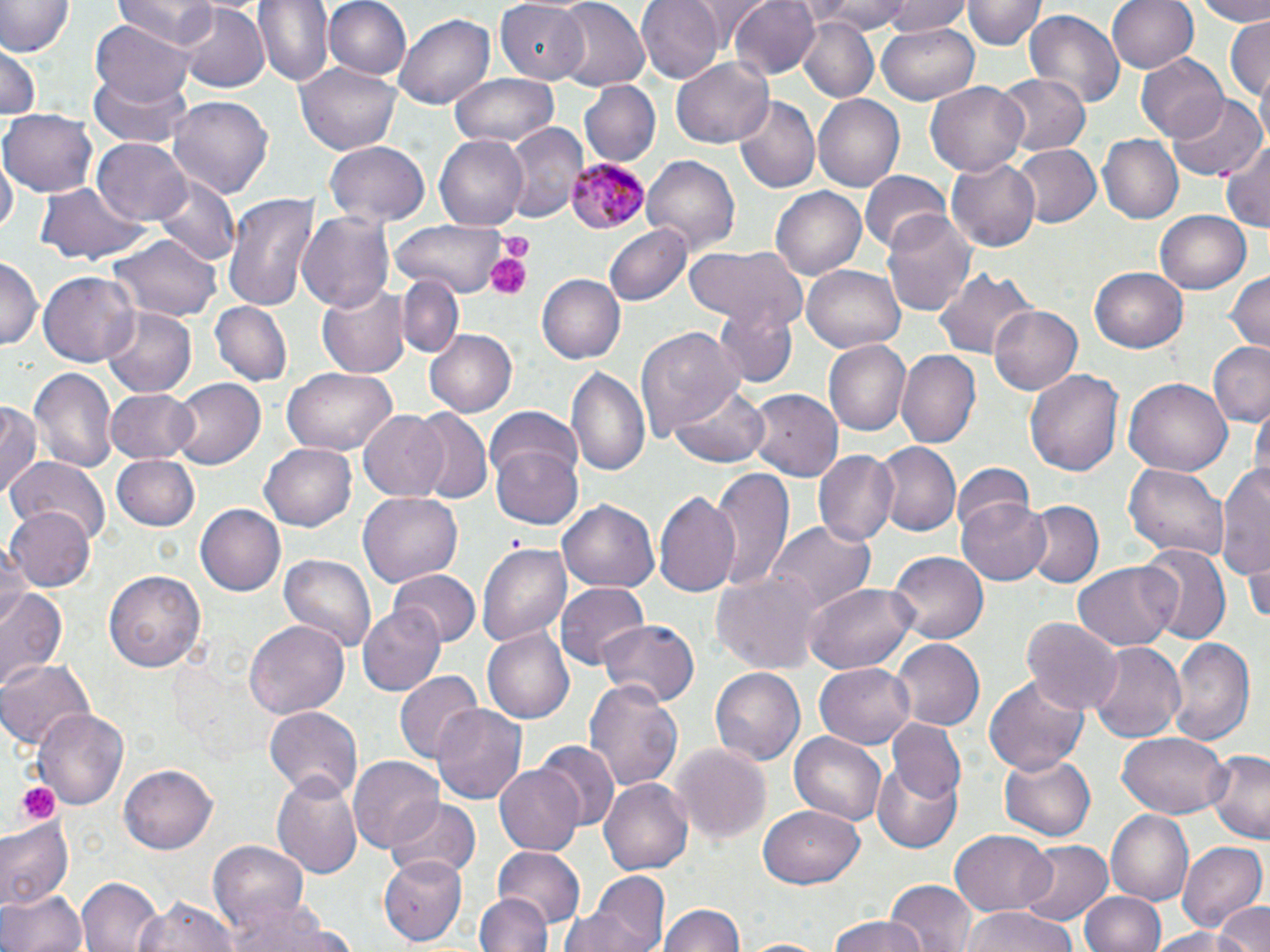
slide-level diagnosis = Plasmodium malariae
modality = light microscopy
magnification = 1000x
Plasmodium malariae-infected red blood cell locations = approximate bounding boxes as (x1, y1, x2, y2) in pixels: (564, 156, 651, 234)
uninfected red blood cell locations = approximate bounding boxes as (x1, y1, x2, y2) in pixels: (116, 0, 220, 46), (255, 0, 334, 86), (326, 0, 411, 80), (637, 0, 721, 84), (690, 0, 770, 42), (729, 0, 819, 80), (805, 0, 914, 34), (879, 0, 973, 37), (965, 0, 1044, 51), (1107, 0, 1198, 74), (1188, 0, 1270, 25), (0, 1, 73, 58), (496, 2, 591, 80), (551, 2, 651, 93), (178, 6, 271, 92), (1024, 9, 1125, 110), (393, 11, 497, 112), (1226, 16, 1269, 105), (796, 18, 877, 102), (91, 20, 193, 112), (876, 21, 980, 103), (1, 46, 40, 121), (1136, 54, 1229, 141), (672, 58, 773, 149), (297, 62, 400, 154), (90, 67, 192, 152), (450, 74, 559, 147), (997, 74, 1088, 155), (579, 80, 661, 166), (925, 80, 1030, 177), (167, 95, 275, 200), (733, 96, 820, 195), (815, 96, 904, 191), (1167, 96, 1263, 181), (3, 107, 98, 197), (504, 122, 586, 221), (434, 134, 527, 230), (1099, 135, 1182, 223), (94, 138, 192, 226), (324, 140, 430, 226), (1219, 140, 1270, 233), (1010, 144, 1100, 228), (1, 155, 16, 245), (643, 155, 740, 252), (946, 158, 1040, 251), (861, 171, 953, 255), (153, 174, 240, 268), (33, 185, 152, 269), (770, 187, 866, 281), (223, 191, 320, 310), (882, 210, 977, 320), (1154, 210, 1253, 294), (297, 211, 396, 314), (393, 216, 514, 299), (604, 224, 689, 308), (113, 233, 217, 320), (684, 243, 805, 331), (0, 256, 42, 349), (802, 262, 908, 353), (932, 267, 1035, 361), (1089, 267, 1188, 354), (1225, 269, 1269, 355), (40, 271, 140, 365), (537, 275, 625, 364), (399, 276, 463, 356), (316, 281, 409, 380), (210, 300, 291, 387), (710, 301, 801, 389), (990, 304, 1082, 395), (103, 307, 197, 396), (637, 324, 743, 438), (422, 328, 518, 417), (822, 340, 912, 438), (1208, 342, 1270, 428), (896, 350, 979, 447), (566, 363, 651, 482), (28, 365, 119, 478), (1026, 366, 1121, 478), (281, 368, 399, 455), (167, 377, 264, 471), (1124, 377, 1231, 476), (669, 383, 769, 467), (106, 388, 200, 463), (749, 388, 843, 480), (1252, 399, 1268, 488), (0, 401, 42, 501), (483, 407, 583, 498), (410, 410, 494, 505), (358, 411, 451, 502), (260, 441, 357, 531), (487, 441, 585, 529), (872, 442, 960, 538), (813, 449, 900, 547), (9, 456, 110, 546), (113, 456, 200, 531), (1124, 463, 1230, 560), (1216, 463, 1269, 584), (950, 465, 1034, 543), (709, 470, 792, 590), (358, 490, 462, 587), (653, 490, 743, 597), (558, 499, 658, 596), (1023, 501, 1101, 588), (959, 502, 1050, 584), (197, 504, 288, 595), (9, 507, 95, 592), (767, 521, 874, 617), (477, 540, 574, 651), (0, 545, 32, 632), (1139, 545, 1230, 646), (888, 551, 989, 642), (279, 554, 377, 656), (1246, 558, 1270, 625), (1074, 563, 1178, 650), (711, 568, 826, 674), (104, 570, 206, 673), (390, 570, 479, 649), (553, 583, 647, 671), (805, 584, 919, 674), (0, 586, 66, 692), (358, 601, 446, 694), (1023, 615, 1124, 717), (596, 619, 700, 708), (246, 621, 349, 719), (484, 628, 575, 724), (1168, 637, 1257, 746), (890, 638, 985, 731), (1088, 641, 1186, 746), (0, 657, 96, 750), (815, 663, 914, 750), (708, 664, 804, 763), (394, 668, 482, 764), (983, 674, 1090, 777), (584, 678, 686, 792), (431, 705, 528, 805), (262, 706, 361, 800), (36, 707, 129, 811), (886, 718, 968, 802), (789, 731, 887, 826), (1117, 732, 1230, 818), (537, 741, 619, 832), (672, 744, 772, 843), (1205, 750, 1270, 844), (1000, 753, 1096, 841), (349, 757, 443, 853), (121, 761, 217, 851), (873, 761, 962, 852), (494, 767, 582, 853), (273, 775, 365, 878), (600, 778, 692, 876), (387, 798, 481, 881), (760, 803, 864, 887), (1106, 810, 1194, 905), (0, 818, 74, 911), (950, 831, 1054, 913), (1015, 839, 1112, 928), (209, 840, 308, 931), (1178, 840, 1268, 932), (492, 847, 585, 930), (378, 853, 467, 943), (566, 871, 670, 952), (77, 876, 165, 952), (884, 879, 977, 952), (0, 887, 89, 952), (475, 890, 552, 952), (1081, 891, 1165, 952), (133, 896, 236, 952), (227, 897, 339, 952), (1215, 901, 1270, 952), (658, 902, 749, 952), (959, 906, 1080, 952), (828, 916, 927, 952), (1145, 926, 1253, 951)
preparation = thin blood film
platelet locations = approximate bounding boxes as (x1, y1, x2, y2) in pixels: (497, 232, 533, 257), (485, 250, 530, 300), (18, 780, 59, 827)
field of view = single
image size = 1270×952 pixels
stain = May-Grünwald-Giemsa